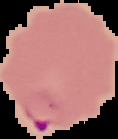

Summary:
  - Image type: segmented cell region on a black background
  - Image size: 118×139 pixels
  - Preparation: thin blood smear
  - Result: malaria parasites identified